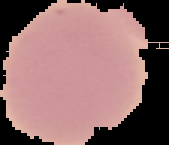 Image is 169×145 pixels. The area outside the segmented cell region is set to black. Malaria status: uninfected. From a thin blood smear.